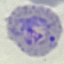
result = malaria parasites detected
image type = cell patch, automatically extracted from a larger field of view and resized to 64 × 64 pixels
capture = smartphone through the microscope eyepiece
preparation = thin blood film
stain = Giemsa